Locate every blood parasite and identify its species.
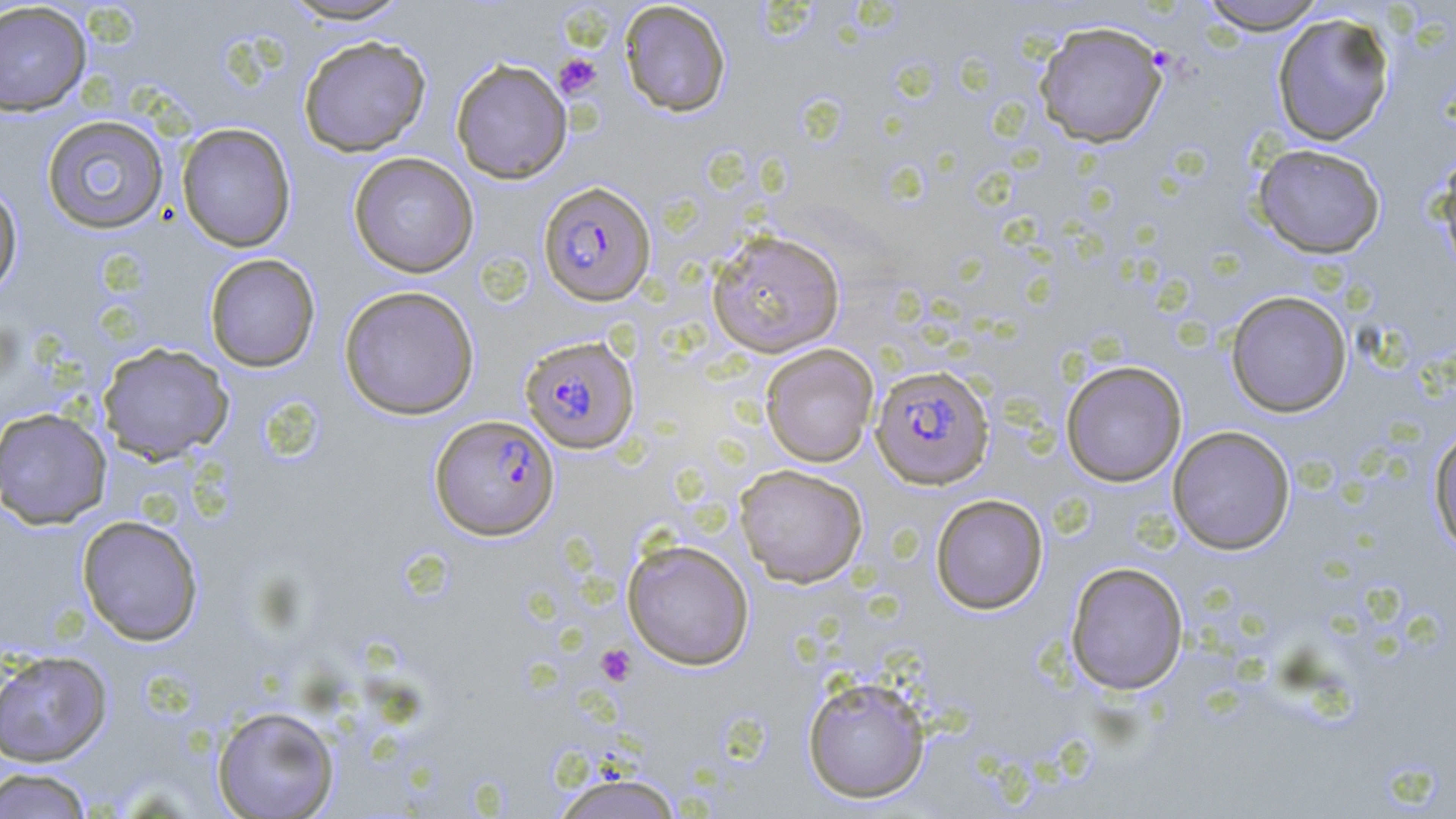

Approximate bounding boxes as [x1, y1, x2, y2] in pixels.
Plasmodium falciparum-infected red blood cells: [538, 181, 656, 306], [519, 335, 640, 454], [870, 365, 995, 489], [431, 414, 560, 540].
No Plasmodium ovale, Plasmodium malariae, Plasmodium vivax, Babesia divergens, or Trypanosoma brucei observed.

Summary:
  - Uninfected red blood cell locations: [277, 0, 415, 25], [1196, 0, 1328, 35], [619, 1, 731, 118], [0, 2, 92, 116], [1271, 12, 1396, 146], [1034, 21, 1169, 148], [298, 35, 431, 157], [450, 58, 572, 184], [41, 114, 169, 235], [176, 122, 296, 253], [1252, 143, 1386, 258], [1431, 147, 1456, 280], [348, 152, 479, 278], [0, 179, 23, 299], [706, 229, 846, 358], [204, 253, 320, 372], [339, 285, 480, 420], [1225, 290, 1352, 418], [97, 342, 233, 464], [760, 343, 879, 467], [1060, 360, 1187, 487], [0, 407, 112, 530], [1428, 424, 1456, 556], [1167, 426, 1295, 554], [734, 463, 868, 588], [930, 494, 1048, 614], [76, 515, 204, 646], [622, 539, 755, 670], [1065, 561, 1188, 695], [0, 650, 113, 766], [802, 674, 931, 803], [211, 705, 340, 819], [1, 767, 95, 818], [548, 772, 687, 819]
  - Platelet locations: [554, 53, 602, 98], [596, 644, 637, 686]
  - Slide-level diagnosis: Plasmodium falciparum
  - Modality: light microscopy
  - Magnification: 1000x
  - Preparation: thin blood smear
  - Field of view: single
  - Image size: 1456×819 pixels
  - Stain: May-Grünwald-Giemsa